Describe the morphology of the erythrocytes.
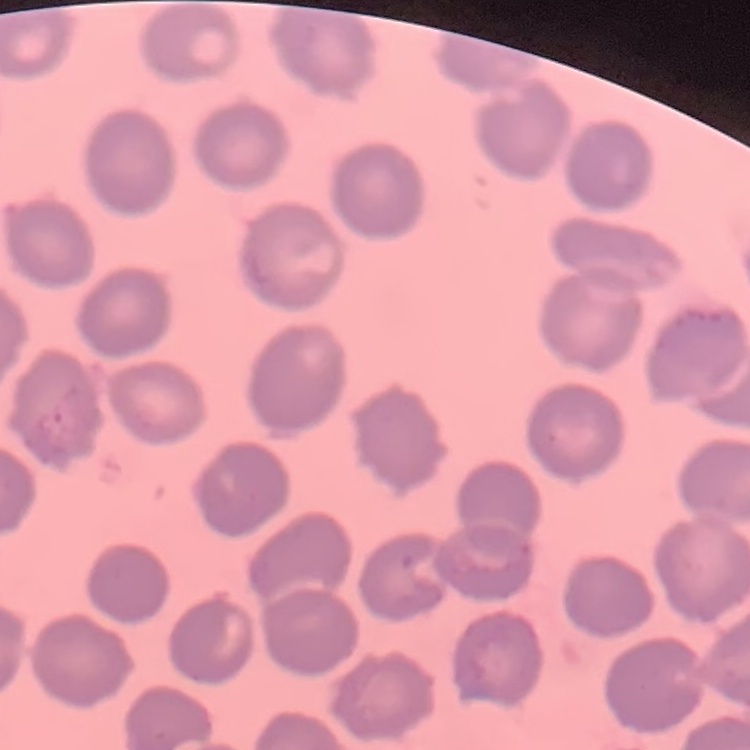

They show no rouleaux formation.

One tile cut from a larger photomicrograph. Thin blood smear. Field's or Giemsa stain.